Locate and identify every blood parasite.
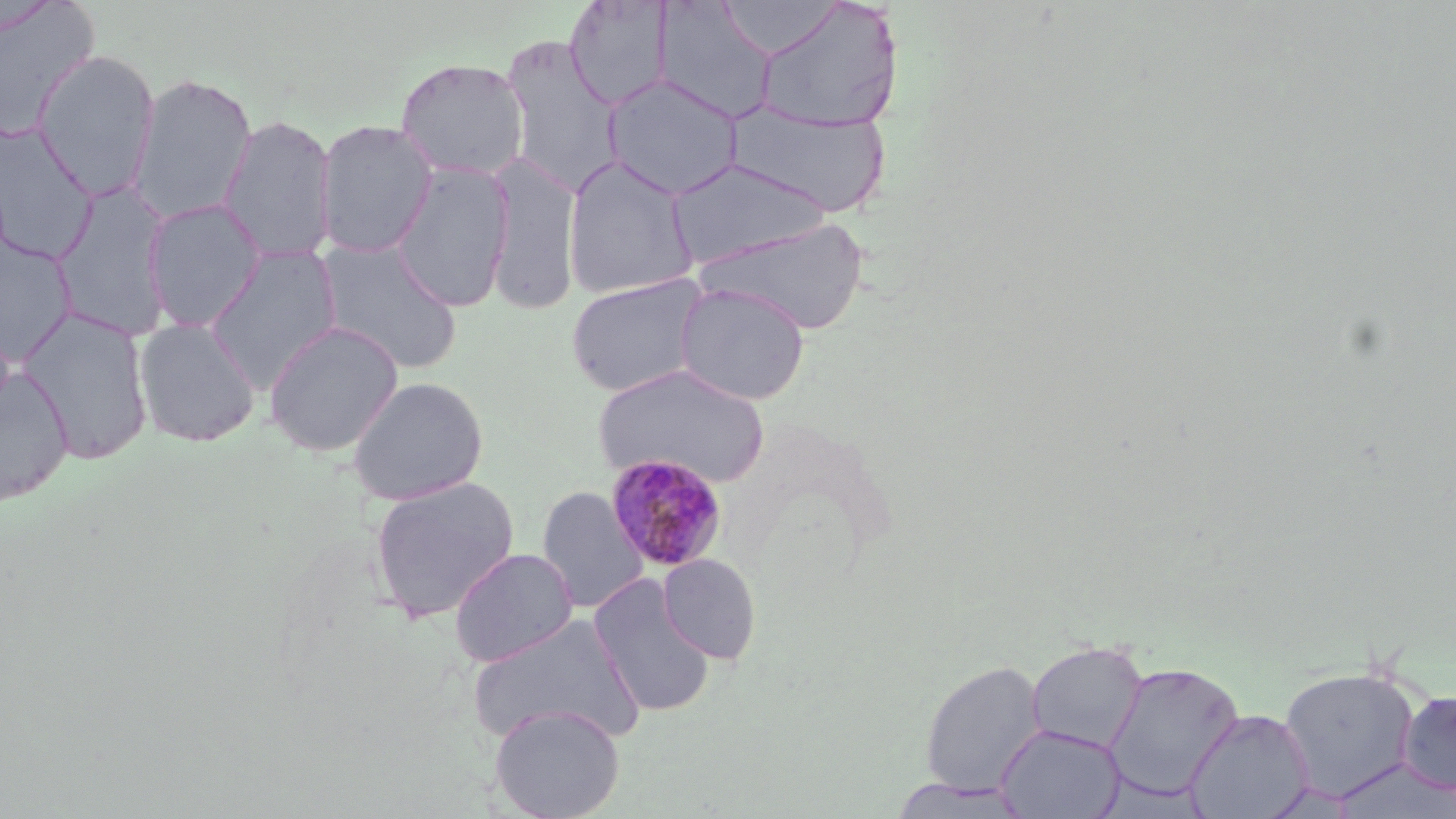

Approximate bounding boxes as [x1, y1, x2, y2] in pixels.
Plasmodium malariae-infected red blood cells: [603, 453, 729, 573].
No Plasmodium falciparum, Plasmodium ovale, Plasmodium vivax, Babesia divergens, or Trypanosoma brucei observed.

slide-level diagnosis = Plasmodium malariae
uninfected red blood cell locations = approximate bounding boxes as [x1, y1, x2, y2] in pixels: [563, 1, 675, 110], [652, 1, 776, 124], [0, 2, 100, 142], [753, 2, 901, 132], [499, 36, 625, 196], [32, 49, 160, 200], [395, 57, 530, 181], [128, 73, 256, 226], [601, 73, 743, 200], [726, 101, 893, 217], [219, 115, 337, 263], [315, 119, 439, 259], [0, 120, 98, 263], [485, 152, 582, 314], [562, 154, 699, 300], [666, 159, 830, 269], [390, 162, 515, 313], [51, 181, 174, 342], [143, 199, 267, 333], [696, 217, 871, 334], [0, 233, 78, 365], [315, 238, 463, 374], [204, 245, 343, 391], [566, 273, 710, 398], [673, 282, 810, 405], [17, 304, 154, 466], [134, 316, 260, 448], [263, 320, 404, 456], [593, 363, 770, 489], [0, 367, 74, 507], [347, 375, 489, 505], [368, 476, 519, 623], [537, 485, 649, 614], [449, 547, 578, 667], [658, 553, 762, 664], [589, 577, 716, 717], [465, 614, 645, 748], [1026, 640, 1148, 754], [919, 659, 1046, 797], [1102, 661, 1244, 801], [1277, 665, 1421, 801], [1397, 690, 1456, 795], [489, 704, 625, 819], [1184, 707, 1314, 819], [995, 723, 1125, 818], [1331, 757, 1456, 818], [888, 778, 1033, 817]
modality = optical microscopy
preparation = thin blood smear
magnification = 1000x
image size = 1456×819 pixels
field of view = one of a larger specimen
stain = May-Grünwald-Giemsa